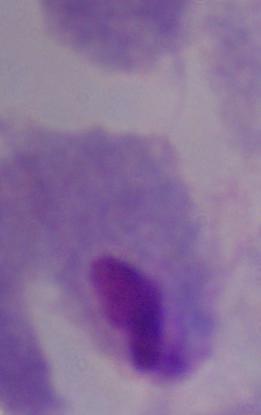

A trichomonad is shown. 1000x magnification. Photomicrograph.